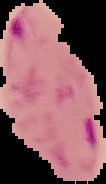

image type = cell region segmented out of the field of view; surrounding area masked to black
image size = 106×184 pixels
preparation = thin blood smear
result = Plasmodium parasites detected